State which parasite is depicted.
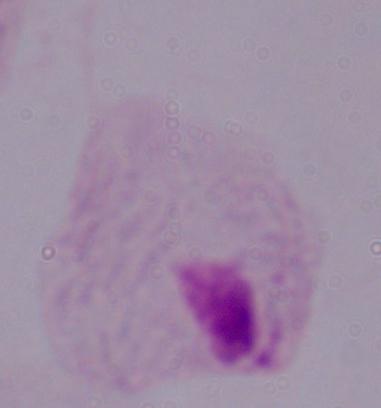

A trichomonad.

Photomicrograph. Captured at 1000x magnification.